Give the extent of all Plasmodium falciparum-infected red blood cells.
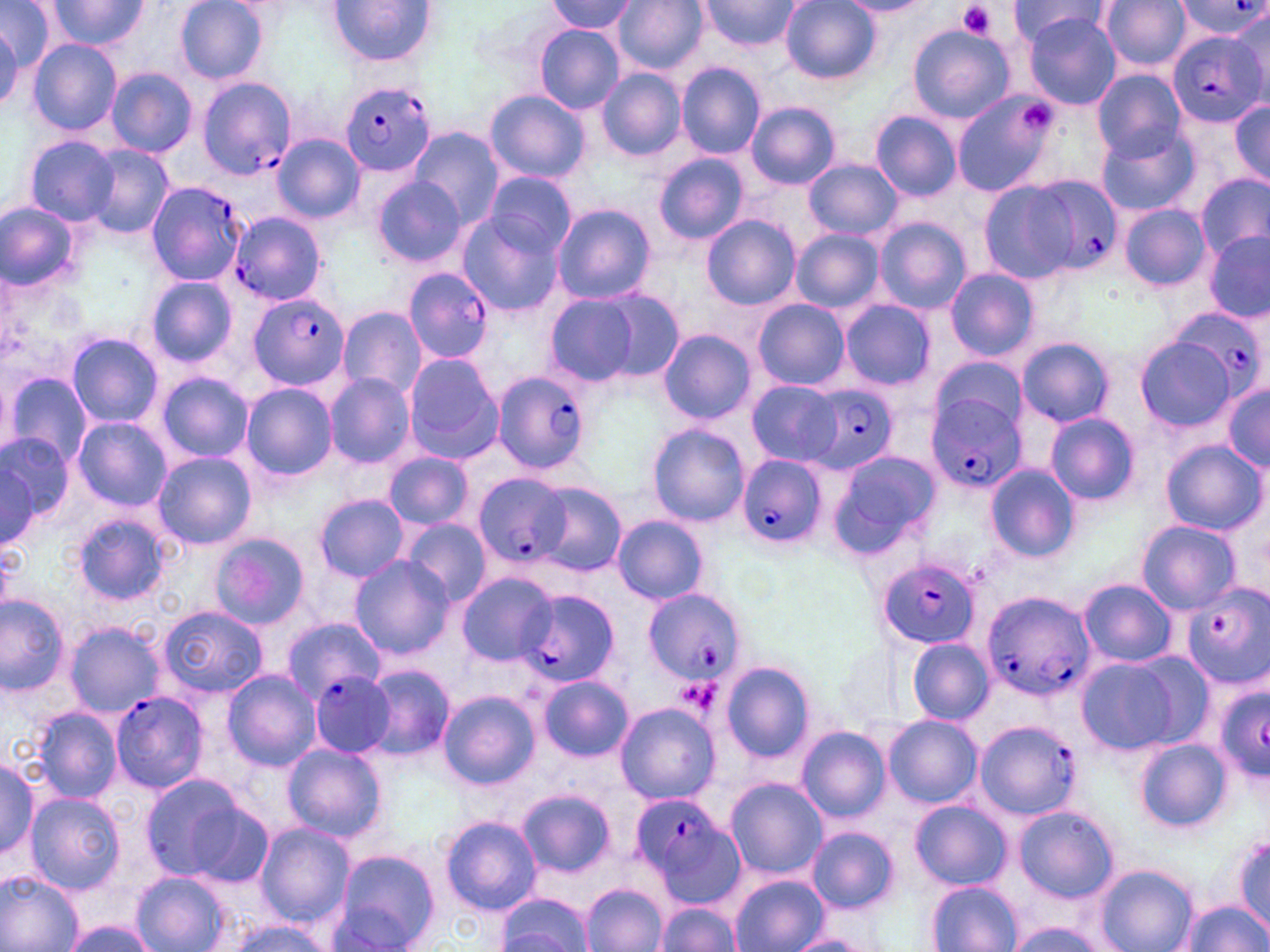

Approximate bounding boxes as named x1/y1/x2/y2 corners in pixels.
Plasmodium falciparum-infected red blood cells: (x1=1174, y1=3, x2=1268, y2=42), (x1=1168, y1=32, x2=1266, y2=127), (x1=196, y1=78, x2=293, y2=180), (x1=342, y1=83, x2=435, y2=177), (x1=1025, y1=176, x2=1125, y2=278), (x1=146, y1=182, x2=251, y2=304), (x1=228, y1=211, x2=326, y2=306), (x1=403, y1=267, x2=495, y2=361), (x1=247, y1=292, x2=349, y2=392), (x1=1173, y1=307, x2=1263, y2=400), (x1=491, y1=370, x2=593, y2=474), (x1=803, y1=383, x2=900, y2=473), (x1=927, y1=394, x2=1026, y2=494), (x1=737, y1=455, x2=825, y2=550), (x1=473, y1=472, x2=575, y2=570), (x1=879, y1=558, x2=981, y2=648), (x1=1182, y1=584, x2=1269, y2=690), (x1=980, y1=589, x2=1095, y2=701), (x1=646, y1=590, x2=742, y2=686), (x1=515, y1=591, x2=622, y2=692), (x1=309, y1=673, x2=395, y2=757), (x1=1214, y1=685, x2=1270, y2=781), (x1=110, y1=690, x2=210, y2=791), (x1=975, y1=720, x2=1080, y2=819), (x1=631, y1=791, x2=740, y2=902).

slide-level diagnosis = Plasmodium falciparum
magnification = 1000x
stain = May-Grünwald-Giemsa
uninfected red blood cell locations = approximate bounding boxes as named x1/y1/x2/y2 corners in pixels: (x1=0, y1=0, x2=58, y2=72), (x1=176, y1=0, x2=267, y2=84), (x1=328, y1=0, x2=437, y2=67), (x1=613, y1=0, x2=708, y2=74), (x1=700, y1=0, x2=801, y2=50), (x1=1099, y1=0, x2=1192, y2=73), (x1=44, y1=1, x2=152, y2=51), (x1=547, y1=1, x2=637, y2=35), (x1=783, y1=1, x2=878, y2=84), (x1=839, y1=1, x2=933, y2=17), (x1=1007, y1=1, x2=1108, y2=48), (x1=1231, y1=6, x2=1268, y2=98), (x1=1024, y1=13, x2=1120, y2=111), (x1=0, y1=22, x2=21, y2=111), (x1=536, y1=25, x2=624, y2=111), (x1=909, y1=26, x2=1015, y2=121), (x1=27, y1=39, x2=122, y2=136), (x1=677, y1=63, x2=766, y2=159), (x1=105, y1=68, x2=196, y2=157), (x1=597, y1=69, x2=686, y2=160), (x1=1092, y1=70, x2=1185, y2=162), (x1=486, y1=90, x2=591, y2=183), (x1=952, y1=94, x2=1057, y2=196), (x1=1228, y1=99, x2=1270, y2=185), (x1=747, y1=101, x2=840, y2=190), (x1=871, y1=112, x2=961, y2=200), (x1=409, y1=126, x2=502, y2=230), (x1=1099, y1=128, x2=1199, y2=216), (x1=274, y1=133, x2=363, y2=224), (x1=25, y1=136, x2=119, y2=225), (x1=82, y1=145, x2=174, y2=239), (x1=654, y1=154, x2=748, y2=245), (x1=805, y1=159, x2=902, y2=240), (x1=483, y1=171, x2=576, y2=261), (x1=1198, y1=173, x2=1270, y2=260), (x1=372, y1=175, x2=465, y2=267), (x1=978, y1=181, x2=1080, y2=283), (x1=1, y1=200, x2=79, y2=290), (x1=552, y1=204, x2=655, y2=305), (x1=1120, y1=204, x2=1211, y2=291), (x1=455, y1=211, x2=563, y2=318), (x1=703, y1=217, x2=799, y2=310), (x1=873, y1=218, x2=971, y2=313), (x1=792, y1=230, x2=883, y2=314), (x1=1205, y1=233, x2=1270, y2=322), (x1=944, y1=268, x2=1038, y2=361), (x1=146, y1=278, x2=239, y2=367), (x1=586, y1=285, x2=686, y2=386), (x1=543, y1=296, x2=638, y2=385), (x1=838, y1=297, x2=935, y2=391), (x1=752, y1=298, x2=849, y2=391), (x1=338, y1=307, x2=426, y2=401), (x1=658, y1=330, x2=755, y2=424), (x1=67, y1=334, x2=163, y2=429), (x1=1017, y1=338, x2=1113, y2=427), (x1=1136, y1=338, x2=1235, y2=432), (x1=403, y1=352, x2=505, y2=463), (x1=928, y1=356, x2=1029, y2=446), (x1=156, y1=372, x2=252, y2=465), (x1=6, y1=373, x2=92, y2=468), (x1=325, y1=373, x2=415, y2=469), (x1=747, y1=379, x2=845, y2=467), (x1=1222, y1=382, x2=1270, y2=468), (x1=241, y1=383, x2=338, y2=482), (x1=1045, y1=412, x2=1139, y2=504), (x1=73, y1=417, x2=170, y2=510), (x1=646, y1=424, x2=751, y2=526), (x1=1, y1=435, x2=74, y2=526), (x1=1162, y1=441, x2=1263, y2=532), (x1=829, y1=449, x2=941, y2=558), (x1=153, y1=452, x2=255, y2=549), (x1=384, y1=452, x2=473, y2=529), (x1=1, y1=462, x2=39, y2=549), (x1=985, y1=464, x2=1079, y2=562), (x1=532, y1=481, x2=627, y2=578), (x1=314, y1=495, x2=410, y2=582), (x1=72, y1=513, x2=171, y2=605), (x1=612, y1=516, x2=708, y2=605), (x1=400, y1=518, x2=491, y2=608), (x1=1137, y1=521, x2=1240, y2=613), (x1=211, y1=534, x2=310, y2=627), (x1=349, y1=555, x2=453, y2=661), (x1=455, y1=571, x2=557, y2=668), (x1=1079, y1=578, x2=1176, y2=667), (x1=0, y1=596, x2=69, y2=694), (x1=158, y1=606, x2=267, y2=698), (x1=280, y1=619, x2=384, y2=704), (x1=64, y1=621, x2=165, y2=716), (x1=906, y1=638, x2=992, y2=724), (x1=1075, y1=658, x2=1183, y2=753), (x1=721, y1=663, x2=814, y2=762), (x1=359, y1=664, x2=454, y2=761), (x1=220, y1=670, x2=321, y2=771), (x1=538, y1=676, x2=633, y2=762), (x1=438, y1=692, x2=540, y2=789), (x1=614, y1=705, x2=719, y2=804), (x1=30, y1=706, x2=122, y2=801), (x1=617, y1=706, x2=719, y2=831), (x1=884, y1=716, x2=981, y2=808), (x1=797, y1=725, x2=889, y2=823), (x1=1134, y1=738, x2=1229, y2=832), (x1=282, y1=744, x2=386, y2=843), (x1=0, y1=753, x2=40, y2=864), (x1=140, y1=773, x2=255, y2=884), (x1=726, y1=779, x2=825, y2=881), (x1=518, y1=789, x2=615, y2=878), (x1=24, y1=793, x2=125, y2=895), (x1=910, y1=800, x2=1010, y2=890), (x1=1015, y1=807, x2=1118, y2=902), (x1=439, y1=815, x2=540, y2=915), (x1=253, y1=823, x2=354, y2=928), (x1=807, y1=826, x2=897, y2=913), (x1=1233, y1=836, x2=1269, y2=929), (x1=328, y1=850, x2=441, y2=952), (x1=1096, y1=864, x2=1196, y2=952), (x1=0, y1=870, x2=83, y2=952), (x1=132, y1=871, x2=231, y2=952), (x1=730, y1=875, x2=828, y2=952), (x1=927, y1=881, x2=1021, y2=952), (x1=582, y1=883, x2=666, y2=952), (x1=497, y1=892, x2=595, y2=952), (x1=1178, y1=900, x2=1268, y2=952), (x1=656, y1=904, x2=740, y2=950), (x1=219, y1=918, x2=332, y2=952), (x1=1012, y1=918, x2=1105, y2=952), (x1=60, y1=920, x2=158, y2=952), (x1=784, y1=934, x2=872, y2=952)
modality = optical microscopy
platelet locations = approximate bounding boxes as named x1/y1/x2/y2 corners in pixels: (x1=956, y1=2, x2=999, y2=39), (x1=1019, y1=100, x2=1057, y2=133)
image size = 1270×952 pixels
preparation = thin blood film
field of view = single